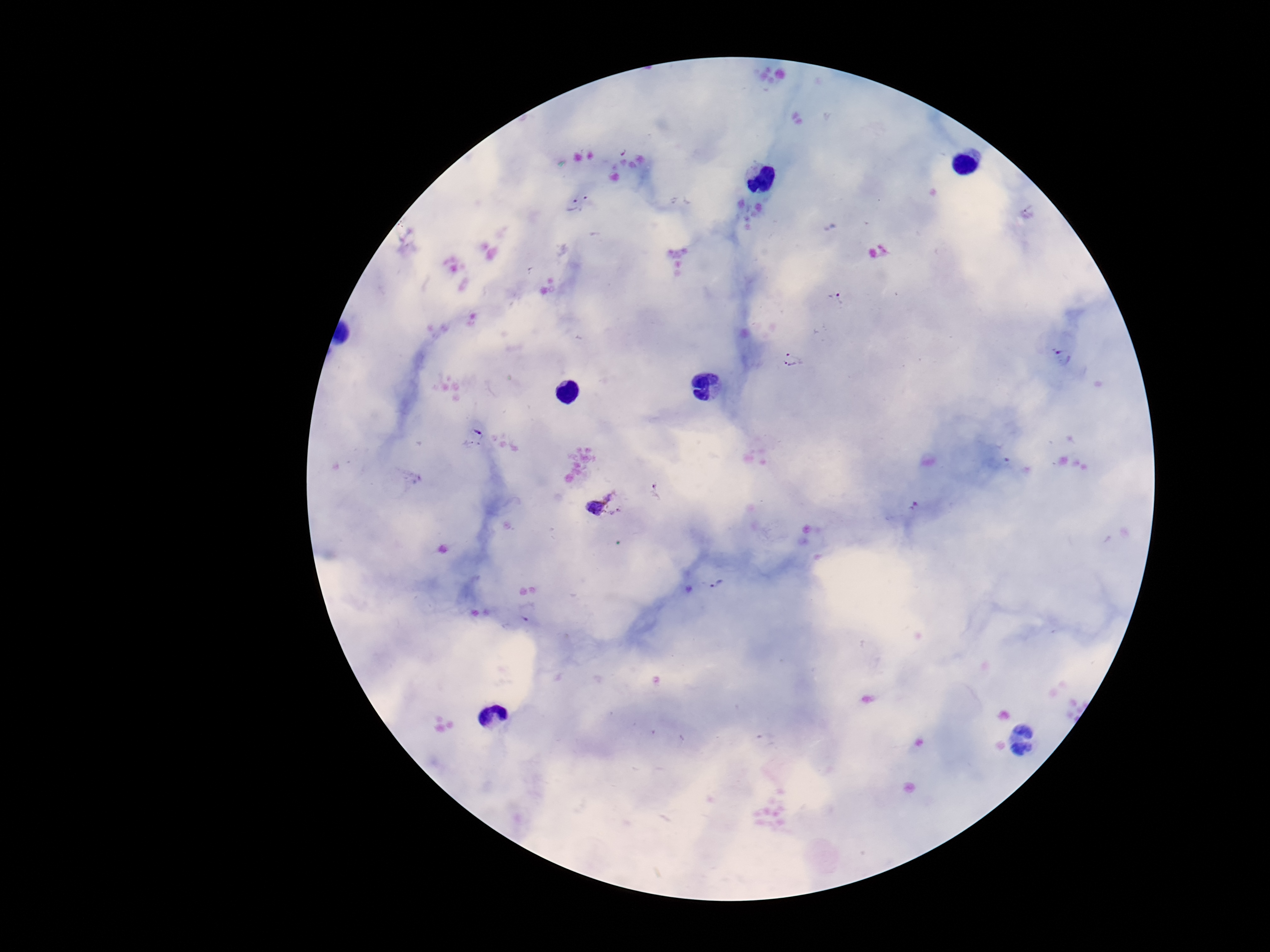
Approximate centers as [x, y] in pixels. Plasmodium parasite locations: [580, 203], [836, 297], [1063, 357], [790, 360], [473, 438], [412, 476], [656, 493], [601, 502], [714, 584], [528, 611]. Thick blood film. Image is 1270×952 pixels. Patient malaria status: positive. 100x magnification. Photographed through the microscope eyepiece with a smartphone camera. One field from this slide. Giemsa-stained preparation.